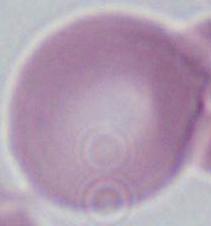

1000x magnification. Micrograph. A red blood cell is shown.